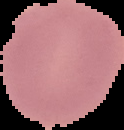 Image is 124×130 pixels. From a thin blood smear. Result: no Plasmodium parasites seen. Cell region segmented out of the field of view; the surrounding area is masked to black.